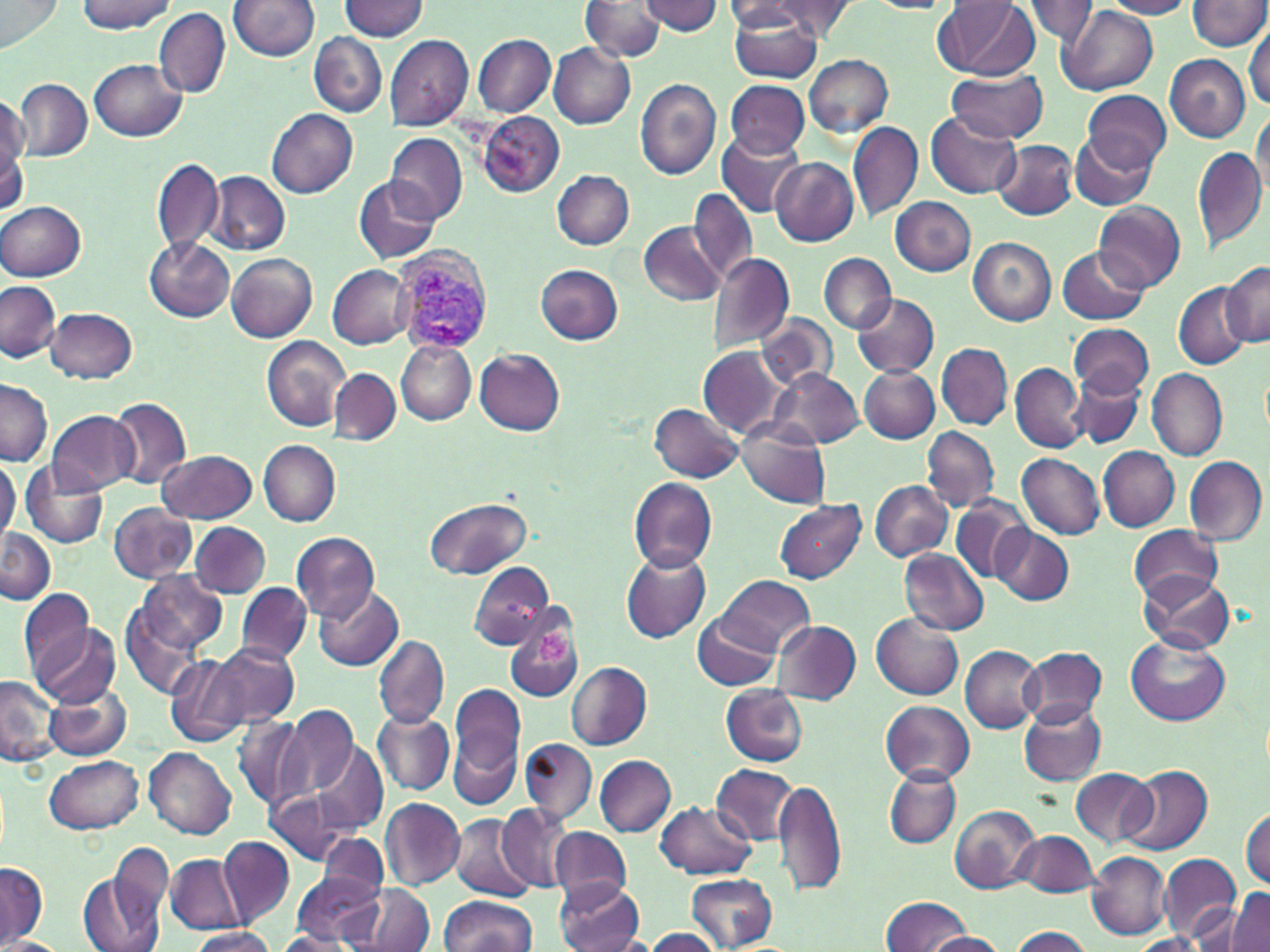 Approximate bounding boxes as named x1/y1/x2/y2 corners in pixels. Uninfected red blood cell locations: (x1=0, y1=0, x2=63, y2=51), (x1=77, y1=0, x2=175, y2=33), (x1=340, y1=0, x2=430, y2=40), (x1=940, y1=0, x2=1039, y2=80), (x1=1021, y1=0, x2=1100, y2=46), (x1=1103, y1=0, x2=1196, y2=19), (x1=229, y1=1, x2=319, y2=61), (x1=582, y1=1, x2=664, y2=61), (x1=601, y1=1, x2=711, y2=52), (x1=637, y1=1, x2=723, y2=36), (x1=769, y1=1, x2=856, y2=38), (x1=864, y1=1, x2=956, y2=14), (x1=724, y1=2, x2=810, y2=33), (x1=1187, y1=2, x2=1269, y2=51), (x1=728, y1=6, x2=822, y2=84), (x1=1060, y1=7, x2=1158, y2=96), (x1=155, y1=8, x2=230, y2=98), (x1=1245, y1=27, x2=1269, y2=110), (x1=308, y1=32, x2=386, y2=116), (x1=472, y1=34, x2=555, y2=117), (x1=385, y1=35, x2=473, y2=130), (x1=548, y1=45, x2=636, y2=129), (x1=803, y1=54, x2=895, y2=138), (x1=1165, y1=54, x2=1250, y2=142), (x1=90, y1=59, x2=185, y2=141), (x1=944, y1=67, x2=1047, y2=142), (x1=14, y1=78, x2=91, y2=161), (x1=635, y1=79, x2=722, y2=181), (x1=724, y1=79, x2=812, y2=157), (x1=1083, y1=89, x2=1171, y2=172), (x1=0, y1=94, x2=28, y2=173), (x1=1251, y1=108, x2=1269, y2=196), (x1=267, y1=109, x2=358, y2=199), (x1=477, y1=111, x2=564, y2=197), (x1=925, y1=112, x2=1021, y2=199), (x1=848, y1=120, x2=923, y2=223), (x1=715, y1=129, x2=805, y2=217), (x1=385, y1=131, x2=467, y2=225), (x1=1070, y1=132, x2=1155, y2=210), (x1=994, y1=140, x2=1078, y2=220), (x1=0, y1=144, x2=27, y2=218), (x1=1192, y1=146, x2=1268, y2=252), (x1=152, y1=156, x2=224, y2=256), (x1=772, y1=156, x2=859, y2=246), (x1=552, y1=170, x2=634, y2=250), (x1=208, y1=171, x2=290, y2=256), (x1=353, y1=176, x2=441, y2=264), (x1=688, y1=189, x2=755, y2=285), (x1=890, y1=195, x2=976, y2=275), (x1=1, y1=201, x2=87, y2=281), (x1=1096, y1=202, x2=1184, y2=291), (x1=638, y1=221, x2=726, y2=306), (x1=145, y1=238, x2=233, y2=323), (x1=968, y1=238, x2=1055, y2=324), (x1=1057, y1=246, x2=1147, y2=324), (x1=227, y1=252, x2=318, y2=342), (x1=820, y1=252, x2=897, y2=334), (x1=707, y1=253, x2=794, y2=351), (x1=1221, y1=263, x2=1270, y2=346), (x1=535, y1=264, x2=623, y2=345), (x1=328, y1=265, x2=415, y2=348), (x1=0, y1=281, x2=61, y2=364), (x1=1173, y1=281, x2=1249, y2=370), (x1=852, y1=294, x2=939, y2=378), (x1=45, y1=308, x2=136, y2=383), (x1=756, y1=315, x2=836, y2=390), (x1=1069, y1=324, x2=1153, y2=399), (x1=262, y1=336, x2=351, y2=432), (x1=396, y1=341, x2=476, y2=424), (x1=936, y1=343, x2=1012, y2=430), (x1=699, y1=345, x2=787, y2=438), (x1=474, y1=348, x2=564, y2=434), (x1=1010, y1=363, x2=1087, y2=453), (x1=860, y1=366, x2=939, y2=444), (x1=329, y1=368, x2=401, y2=444), (x1=769, y1=368, x2=863, y2=448), (x1=1146, y1=368, x2=1227, y2=461), (x1=1073, y1=375, x2=1146, y2=448), (x1=0, y1=378, x2=51, y2=466), (x1=109, y1=398, x2=192, y2=488), (x1=649, y1=404, x2=745, y2=482), (x1=48, y1=411, x2=140, y2=495), (x1=737, y1=424, x2=829, y2=507), (x1=922, y1=426, x2=999, y2=511), (x1=257, y1=438, x2=342, y2=526), (x1=1098, y1=446, x2=1179, y2=531), (x1=160, y1=449, x2=257, y2=522), (x1=1016, y1=453, x2=1105, y2=540), (x1=0, y1=456, x2=19, y2=544), (x1=1185, y1=456, x2=1267, y2=546), (x1=22, y1=463, x2=109, y2=549), (x1=628, y1=477, x2=717, y2=573), (x1=868, y1=479, x2=952, y2=561), (x1=951, y1=496, x2=1035, y2=584), (x1=423, y1=497, x2=532, y2=580), (x1=774, y1=500, x2=865, y2=583), (x1=107, y1=504, x2=196, y2=583), (x1=190, y1=521, x2=270, y2=597), (x1=991, y1=525, x2=1073, y2=604), (x1=1129, y1=526, x2=1223, y2=604), (x1=0, y1=527, x2=54, y2=604), (x1=292, y1=532, x2=380, y2=622), (x1=620, y1=549, x2=710, y2=643), (x1=900, y1=549, x2=987, y2=635), (x1=468, y1=561, x2=554, y2=650), (x1=133, y1=569, x2=227, y2=654), (x1=1137, y1=569, x2=1233, y2=655), (x1=717, y1=575, x2=815, y2=654), (x1=237, y1=582, x2=310, y2=663), (x1=314, y1=586, x2=402, y2=672), (x1=19, y1=587, x2=98, y2=685), (x1=122, y1=604, x2=202, y2=699), (x1=692, y1=613, x2=781, y2=691), (x1=871, y1=615, x2=962, y2=699), (x1=504, y1=618, x2=584, y2=705), (x1=772, y1=620, x2=861, y2=704), (x1=33, y1=622, x2=120, y2=708), (x1=374, y1=634, x2=449, y2=729), (x1=1127, y1=636, x2=1229, y2=726), (x1=212, y1=643, x2=299, y2=727), (x1=960, y1=646, x2=1043, y2=732), (x1=1019, y1=646, x2=1106, y2=724), (x1=165, y1=654, x2=249, y2=749), (x1=565, y1=661, x2=651, y2=750), (x1=0, y1=674, x2=60, y2=767), (x1=448, y1=680, x2=526, y2=792), (x1=44, y1=682, x2=131, y2=760), (x1=720, y1=685, x2=809, y2=767), (x1=881, y1=699, x2=974, y2=784), (x1=284, y1=702, x2=357, y2=801), (x1=1019, y1=703, x2=1105, y2=786), (x1=374, y1=711, x2=453, y2=796), (x1=233, y1=714, x2=309, y2=813), (x1=448, y1=730, x2=520, y2=811), (x1=520, y1=737, x2=596, y2=825), (x1=311, y1=742, x2=388, y2=832), (x1=141, y1=748, x2=235, y2=840), (x1=44, y1=755, x2=145, y2=834), (x1=595, y1=755, x2=677, y2=836), (x1=712, y1=764, x2=798, y2=844), (x1=1122, y1=764, x2=1211, y2=855), (x1=884, y1=767, x2=961, y2=848), (x1=1072, y1=767, x2=1157, y2=847), (x1=772, y1=777, x2=844, y2=897), (x1=266, y1=790, x2=353, y2=864), (x1=381, y1=798, x2=465, y2=889), (x1=657, y1=799, x2=756, y2=879), (x1=496, y1=804, x2=571, y2=890), (x1=950, y1=805, x2=1039, y2=893), (x1=1242, y1=807, x2=1270, y2=888), (x1=450, y1=814, x2=535, y2=902), (x1=552, y1=826, x2=630, y2=904), (x1=1014, y1=829, x2=1099, y2=897), (x1=316, y1=832, x2=389, y2=902), (x1=218, y1=835, x2=294, y2=927), (x1=110, y1=842, x2=173, y2=936), (x1=1086, y1=852, x2=1170, y2=939), (x1=1159, y1=853, x2=1240, y2=940), (x1=166, y1=854, x2=247, y2=934), (x1=79, y1=862, x2=167, y2=952), (x1=1, y1=863, x2=48, y2=944), (x1=685, y1=872, x2=778, y2=951), (x1=292, y1=873, x2=383, y2=945), (x1=554, y1=880, x2=643, y2=951), (x1=355, y1=885, x2=435, y2=951), (x1=1227, y1=889, x2=1270, y2=951), (x1=882, y1=895, x2=969, y2=951), (x1=439, y1=896, x2=535, y2=951), (x1=1192, y1=897, x2=1258, y2=948), (x1=1008, y1=926, x2=1092, y2=951), (x1=187, y1=928, x2=280, y2=952), (x1=644, y1=928, x2=723, y2=951), (x1=272, y1=931, x2=357, y2=952), (x1=925, y1=931, x2=1007, y2=951), (x1=1126, y1=934, x2=1210, y2=951), (x1=0, y1=937, x2=66, y2=952). Plasmodium vivax-infected red blood cell locations: (x1=395, y1=242, x2=495, y2=352). Platelet locations: (x1=537, y1=630, x2=572, y2=666). Slide-level diagnosis: Plasmodium vivax. Thin blood smear. Light microscopy. Image is 1270×952 pixels. May-Grünwald-Giemsa stain. Captured at 1000x magnification. One field of a larger specimen.